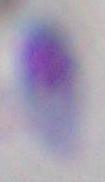

modality: photomicrograph
identification: Toxoplasma gondii
magnification: 1000x